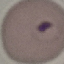
result = malaria parasites identified
stain = Giemsa
capture = smartphone camera at the microscope eyepiece
preparation = thin blood film
image type = cell patch, automatically extracted from a larger field of view and resized to 64 × 64 pixels